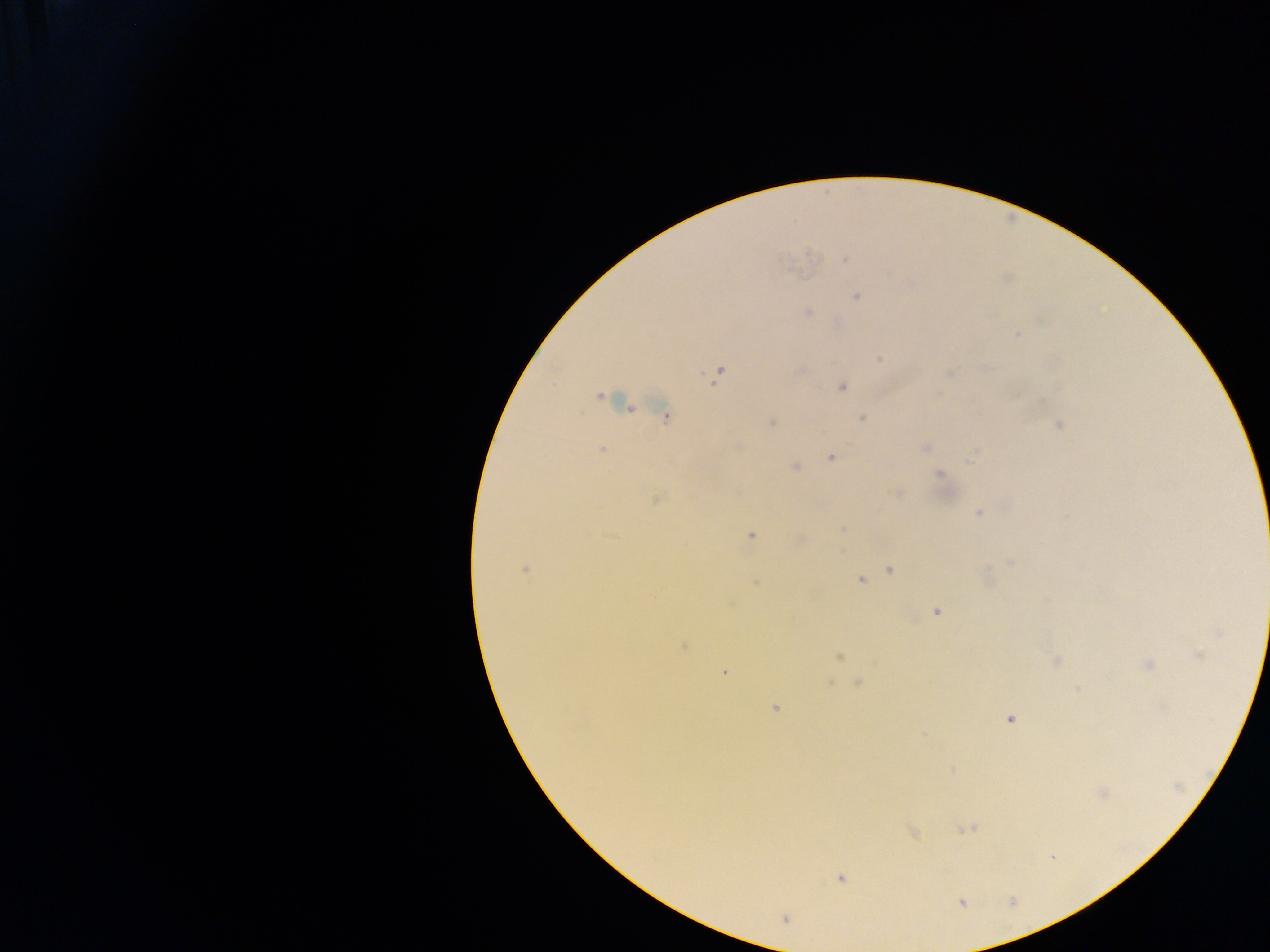
Plasmodium parasite locations = approximate centers as [x, y] in pixels: [845, 260], [856, 296], [809, 312], [1017, 334], [880, 359], [718, 375], [841, 387], [600, 396], [665, 416], [861, 418], [771, 423], [1059, 425], [739, 446], [925, 447], [602, 450], [831, 457], [971, 458], [795, 467], [941, 474], [897, 492], [656, 499], [979, 513], [751, 535], [1010, 562], [525, 570], [891, 570], [860, 580], [936, 612], [1218, 633], [684, 646], [839, 657], [1056, 660], [1147, 664], [723, 672], [858, 683], [1077, 689], [775, 708], [1011, 719], [1102, 793], [968, 828], [913, 833], [840, 878], [962, 903], [785, 920]
preparation = thick blood film
capture = mobile-phone photograph through a microscope
image size = 1270×952 pixels
field of view = single
country = Ghana